Report the malaria status of this cell.
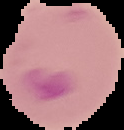
Parasitized.

image_type: segmented cell region with the area outside set to black
preparation: thin blood film
image_size: 124×130 pixels